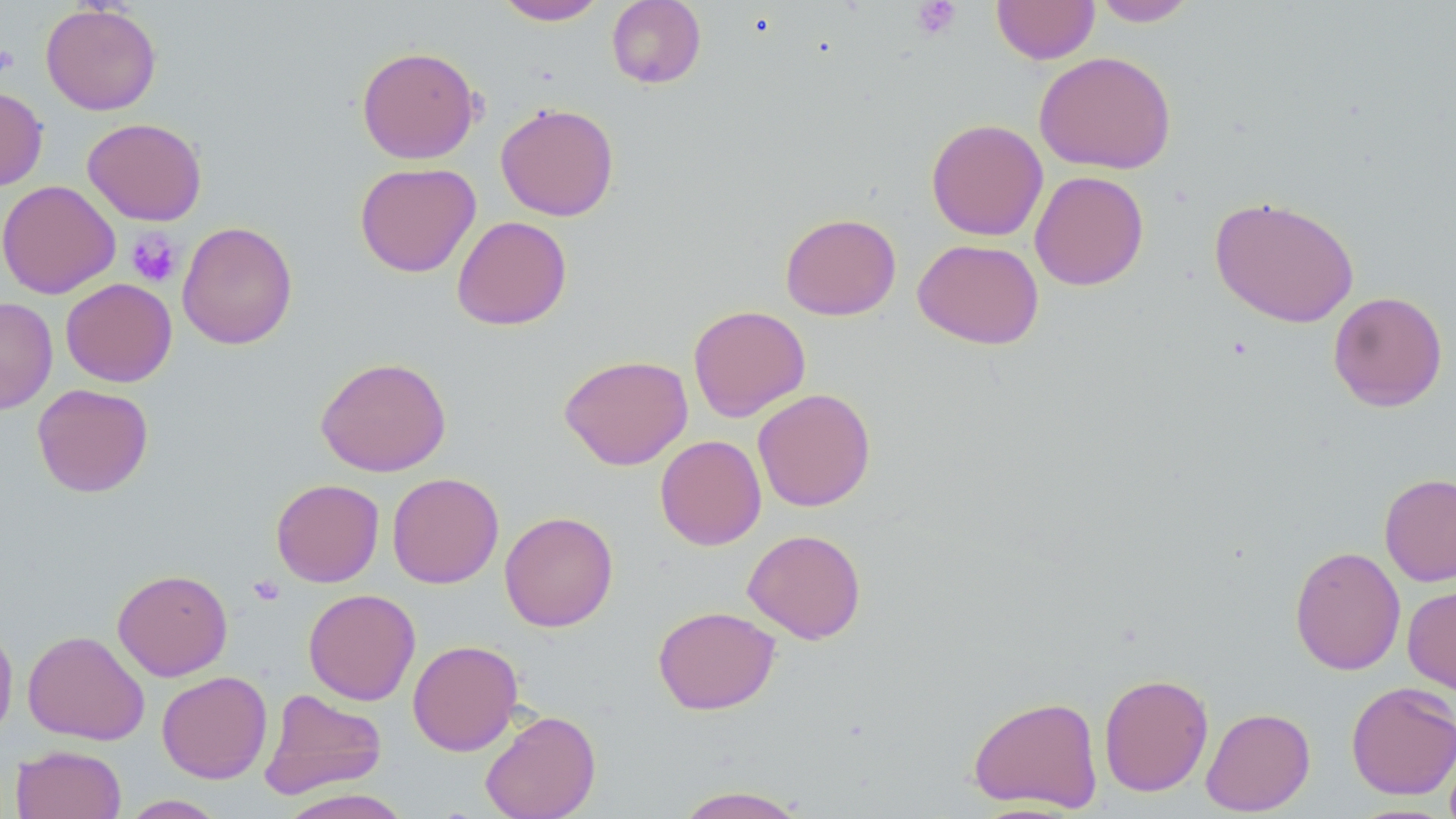
Approximate bounding boxes as [x1, y1, x2, y2] in pixels. Uninfected red blood cell locations: [494, 0, 608, 25], [606, 0, 706, 88], [992, 0, 1099, 64], [1092, 0, 1199, 27], [41, 3, 162, 115], [356, 45, 481, 164], [1034, 51, 1176, 174], [0, 85, 48, 190], [495, 102, 620, 222], [82, 117, 207, 225], [926, 118, 1048, 241], [355, 162, 481, 278], [1029, 170, 1149, 290], [0, 179, 120, 299], [1209, 194, 1359, 328], [780, 212, 901, 321], [451, 215, 572, 330], [177, 221, 298, 350], [913, 238, 1044, 349], [61, 278, 177, 387], [1328, 291, 1448, 412], [0, 297, 58, 414], [687, 304, 811, 422], [559, 354, 693, 470], [315, 356, 452, 477], [32, 383, 154, 497], [752, 388, 876, 512], [655, 434, 767, 550], [387, 472, 504, 588], [1379, 473, 1456, 586], [270, 478, 384, 587], [500, 511, 619, 632], [743, 528, 867, 644], [1289, 545, 1406, 675], [112, 568, 233, 681], [1403, 582, 1456, 696], [303, 588, 420, 706], [653, 605, 780, 715], [0, 618, 18, 744], [23, 630, 149, 745], [407, 639, 523, 756], [157, 670, 272, 784], [1098, 672, 1214, 797], [1345, 682, 1456, 800], [259, 689, 387, 799], [967, 694, 1104, 813], [1201, 707, 1316, 815], [480, 709, 601, 819], [11, 744, 126, 819], [672, 785, 811, 818], [276, 788, 416, 819], [119, 795, 227, 818]. Platelet locations: [911, 1, 961, 39], [0, 46, 18, 75], [126, 230, 182, 288], [248, 574, 285, 606]. Slide-level diagnosis: negative for blood parasites. Optical microscopy. One field of a larger specimen. Thin blood film. Image is 1456×819 pixels. 1000x magnification. May-Grünwald-Giemsa-stained preparation.